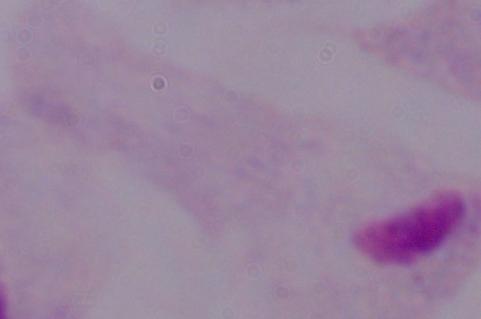 A trichomonad is seen. Micrograph. 1000x magnification.